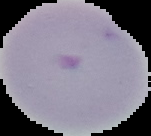
Summary:
  - Image size: 151×136 pixels
  - Malaria status: uninfected
  - Preparation: thin blood smear
  - Image type: segmented cell region with the area outside set to black